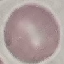

Summary:
  - Result: no malaria parasites detected
  - Image type: cell patch, automatically extracted from a larger field of view and resized to 64 × 64 pixels
  - Capture: smartphone through the microscope eyepiece
  - Stain: Giemsa
  - Preparation: thin blood film